Outline each blood parasite and name the species.
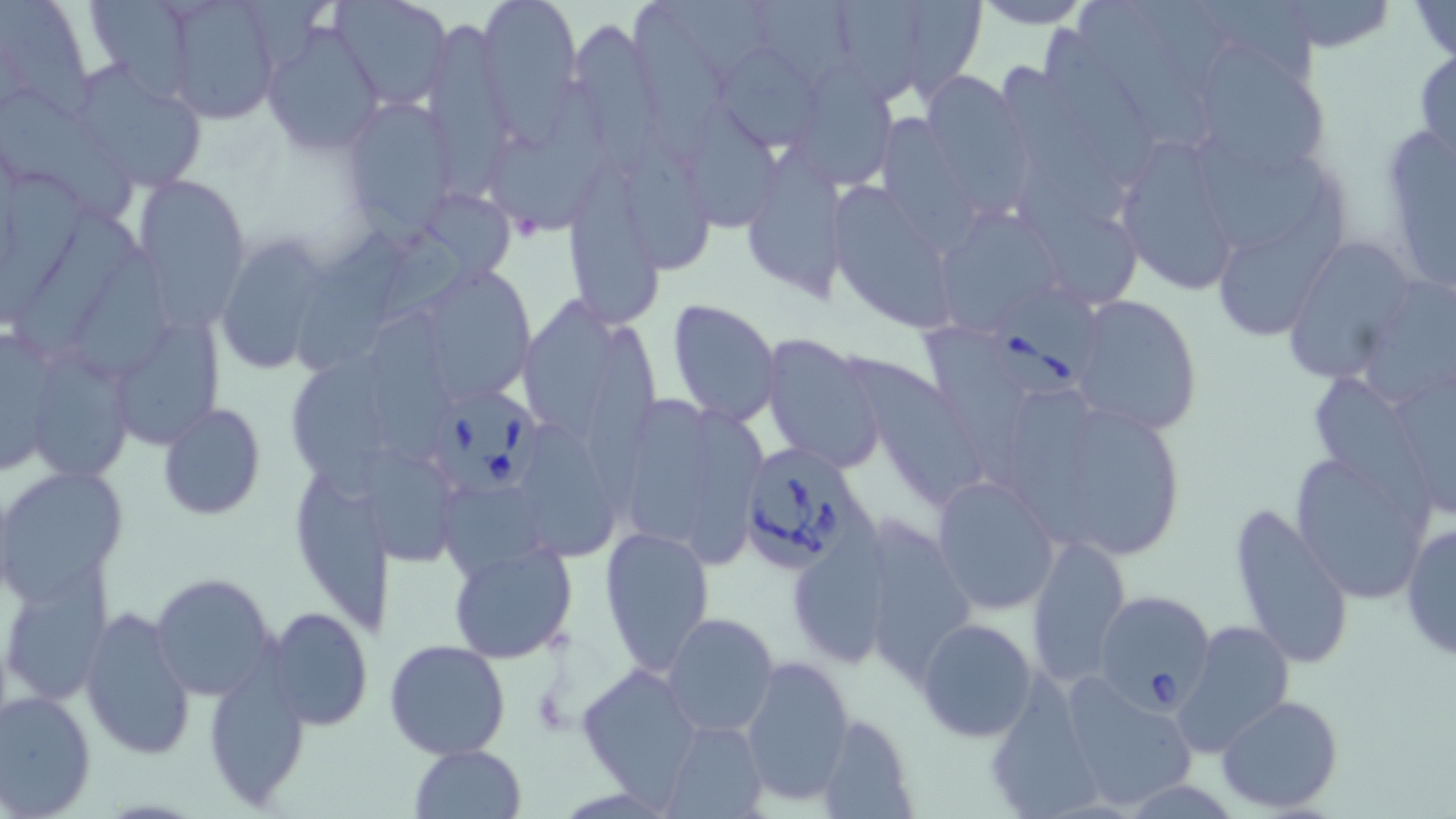

Approximate bounding boxes as [x1, y1, x2, y2] in pixels.
Babesia divergens-infected red blood cells: [987, 290, 1103, 397], [426, 389, 546, 499], [737, 440, 870, 574], [1091, 590, 1214, 712].
No Plasmodium falciparum, Plasmodium ovale, Plasmodium malariae, Plasmodium vivax, or Trypanosoma brucei observed.

Uninfected red blood cell locations: [0, 0, 94, 116], [88, 0, 192, 109], [330, 0, 450, 108], [478, 0, 581, 109], [833, 0, 921, 108], [901, 0, 986, 101], [971, 0, 1095, 28], [1081, 0, 1203, 147], [1198, 0, 1320, 82], [649, 1, 771, 73], [760, 1, 859, 89], [1267, 1, 1404, 54], [1407, 1, 1455, 62], [161, 3, 284, 126], [633, 3, 728, 158], [566, 17, 668, 158], [262, 22, 385, 156], [426, 22, 522, 207], [1045, 24, 1156, 187], [1189, 43, 1335, 175], [719, 45, 820, 154], [1412, 45, 1456, 169], [797, 60, 894, 187], [72, 62, 207, 190], [1002, 63, 1129, 221], [918, 74, 1030, 212], [492, 87, 610, 240], [0, 92, 136, 220], [340, 97, 456, 229], [682, 99, 786, 239], [884, 115, 977, 256], [1378, 119, 1455, 295], [622, 127, 712, 273], [1109, 135, 1249, 293], [1200, 140, 1324, 251], [749, 154, 850, 304], [568, 158, 666, 333], [0, 172, 89, 327], [1220, 172, 1346, 340], [134, 173, 249, 311], [831, 185, 956, 333], [1018, 188, 1145, 307], [385, 191, 520, 323], [15, 204, 136, 358], [945, 204, 1062, 330], [294, 218, 411, 372], [1281, 235, 1420, 382], [212, 237, 334, 373], [77, 249, 180, 385], [410, 265, 537, 404], [1357, 276, 1456, 409], [1070, 292, 1203, 435], [511, 297, 614, 439], [666, 298, 782, 428], [366, 302, 456, 466], [93, 320, 225, 457], [582, 321, 660, 515], [924, 321, 1024, 493], [1, 326, 61, 478], [760, 333, 888, 474], [37, 346, 130, 478], [291, 353, 402, 505], [853, 362, 990, 508], [1388, 369, 1456, 522], [1312, 374, 1434, 526], [1012, 390, 1113, 555], [1011, 392, 1098, 546], [626, 396, 708, 544], [158, 403, 266, 518], [678, 408, 769, 573], [1083, 414, 1180, 557], [520, 422, 622, 567], [1288, 450, 1434, 604], [369, 451, 456, 568], [289, 460, 392, 628], [1, 465, 129, 604], [931, 474, 1061, 614], [442, 486, 552, 578], [1229, 499, 1354, 672], [857, 515, 977, 672], [1400, 518, 1456, 664], [600, 524, 714, 676], [1028, 534, 1131, 684], [788, 536, 897, 667], [447, 540, 579, 665], [150, 573, 278, 703], [1, 574, 113, 704], [79, 605, 198, 759], [264, 606, 373, 731], [663, 612, 779, 737], [916, 617, 1038, 739], [1173, 618, 1296, 755], [384, 637, 512, 759], [740, 656, 853, 804], [203, 662, 313, 810], [575, 664, 704, 797], [1059, 670, 1198, 810], [0, 689, 97, 817], [982, 692, 1105, 817], [1215, 694, 1345, 811], [811, 715, 915, 818], [659, 717, 770, 819], [409, 744, 527, 819]. Slide-level diagnosis: Babesia divergens. Captured at 1000x magnification. Thin blood film. Light microscopy. One field of a larger specimen. Image is 1456×819 pixels. May-Grünwald-Giemsa-stained preparation.